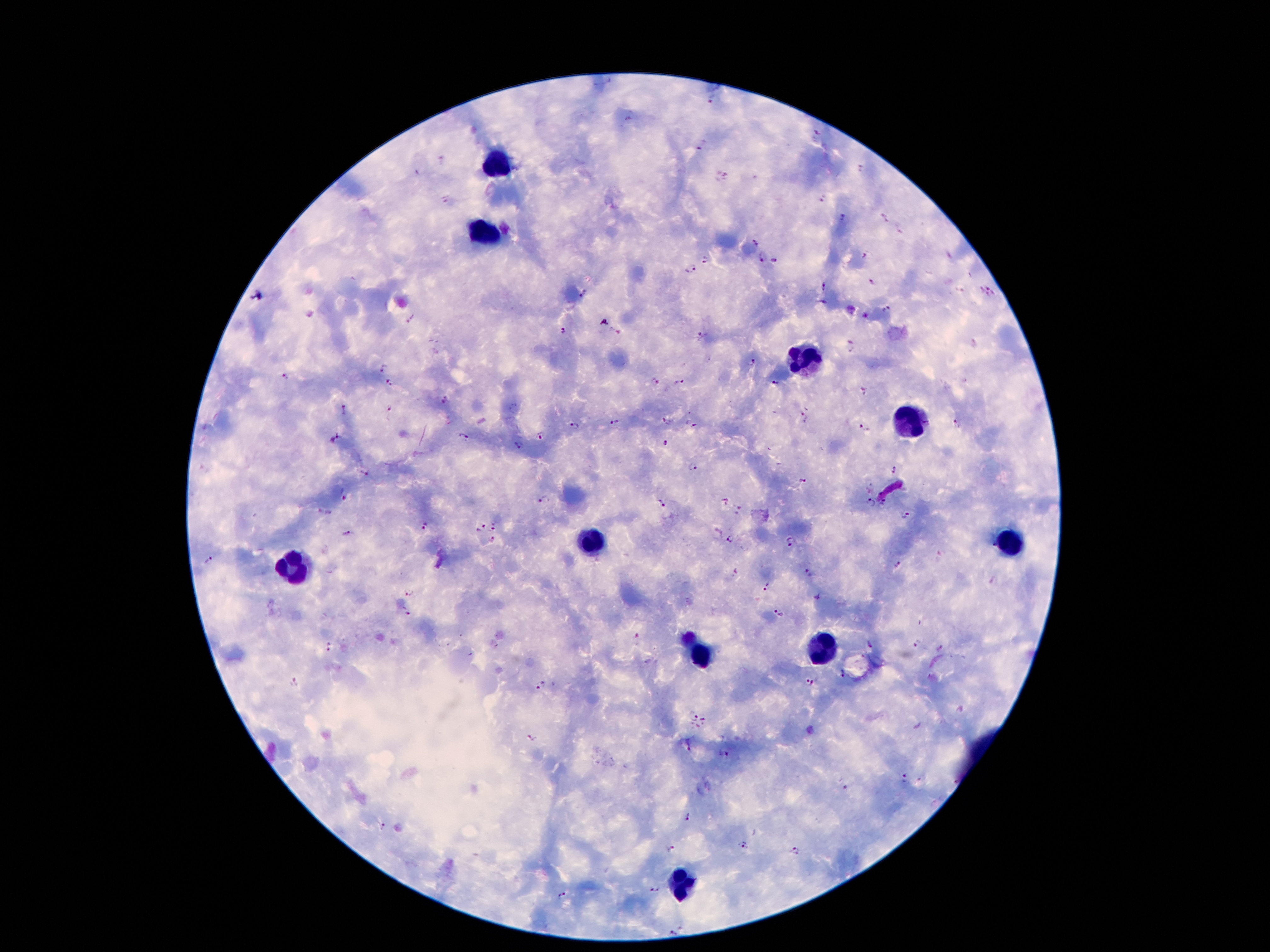
Approximate object centers, in pixels from the top-left corner.
Summary:
  - Plasmodium parasite locations: (x=714, y=99), (x=817, y=133), (x=702, y=146), (x=861, y=169), (x=727, y=175), (x=822, y=197), (x=446, y=201), (x=883, y=217), (x=843, y=218), (x=902, y=229), (x=756, y=242), (x=864, y=255), (x=762, y=258), (x=777, y=258), (x=705, y=259), (x=690, y=269), (x=873, y=282), (x=825, y=285), (x=992, y=286), (x=584, y=294), (x=981, y=294), (x=822, y=304), (x=888, y=309), (x=411, y=319), (x=563, y=333), (x=700, y=336), (x=852, y=346), (x=753, y=362), (x=382, y=369), (x=285, y=378), (x=654, y=382), (x=679, y=382), (x=775, y=382), (x=390, y=384), (x=863, y=391), (x=444, y=401), (x=390, y=410), (x=344, y=411), (x=805, y=419), (x=615, y=422), (x=666, y=422), (x=692, y=425), (x=956, y=425), (x=575, y=426), (x=864, y=427), (x=465, y=436), (x=539, y=436), (x=337, y=439), (x=665, y=444), (x=517, y=445), (x=693, y=466), (x=896, y=470), (x=365, y=471), (x=802, y=480), (x=345, y=497), (x=543, y=499), (x=724, y=502), (x=658, y=503), (x=870, y=504), (x=884, y=504), (x=738, y=510), (x=905, y=516), (x=425, y=524), (x=483, y=526), (x=494, y=527), (x=476, y=531), (x=348, y=534), (x=493, y=540), (x=730, y=540), (x=790, y=544), (x=209, y=559), (x=897, y=565), (x=809, y=572), (x=767, y=587), (x=411, y=591), (x=405, y=612), (x=778, y=615), (x=870, y=645), (x=917, y=645), (x=330, y=647), (x=940, y=650), (x=843, y=676), (x=296, y=681), (x=809, y=684), (x=541, y=686), (x=693, y=716), (x=705, y=718), (x=531, y=738), (x=724, y=753), (x=903, y=778), (x=845, y=786), (x=687, y=817), (x=384, y=827), (x=743, y=844), (x=672, y=850), (x=796, y=852), (x=653, y=890), (x=564, y=895), (x=676, y=932)
  - Leukocyte locations: (x=499, y=162), (x=480, y=233), (x=797, y=360), (x=904, y=418), (x=592, y=539), (x=1010, y=543), (x=291, y=566), (x=820, y=648), (x=700, y=657), (x=682, y=883)
  - Stain: Giemsa
  - Capture: smartphone through the microscope eyepiece
  - Field of view: single
  - Preparation: thick peripheral-blood smear
  - Magnification: 100x
  - Image size: 1270×952 pixels
  - Patient malaria status: infected with Plasmodium falciparum